Locate the P. falciparum-infected red blood cells and any of indeterminate infection status.
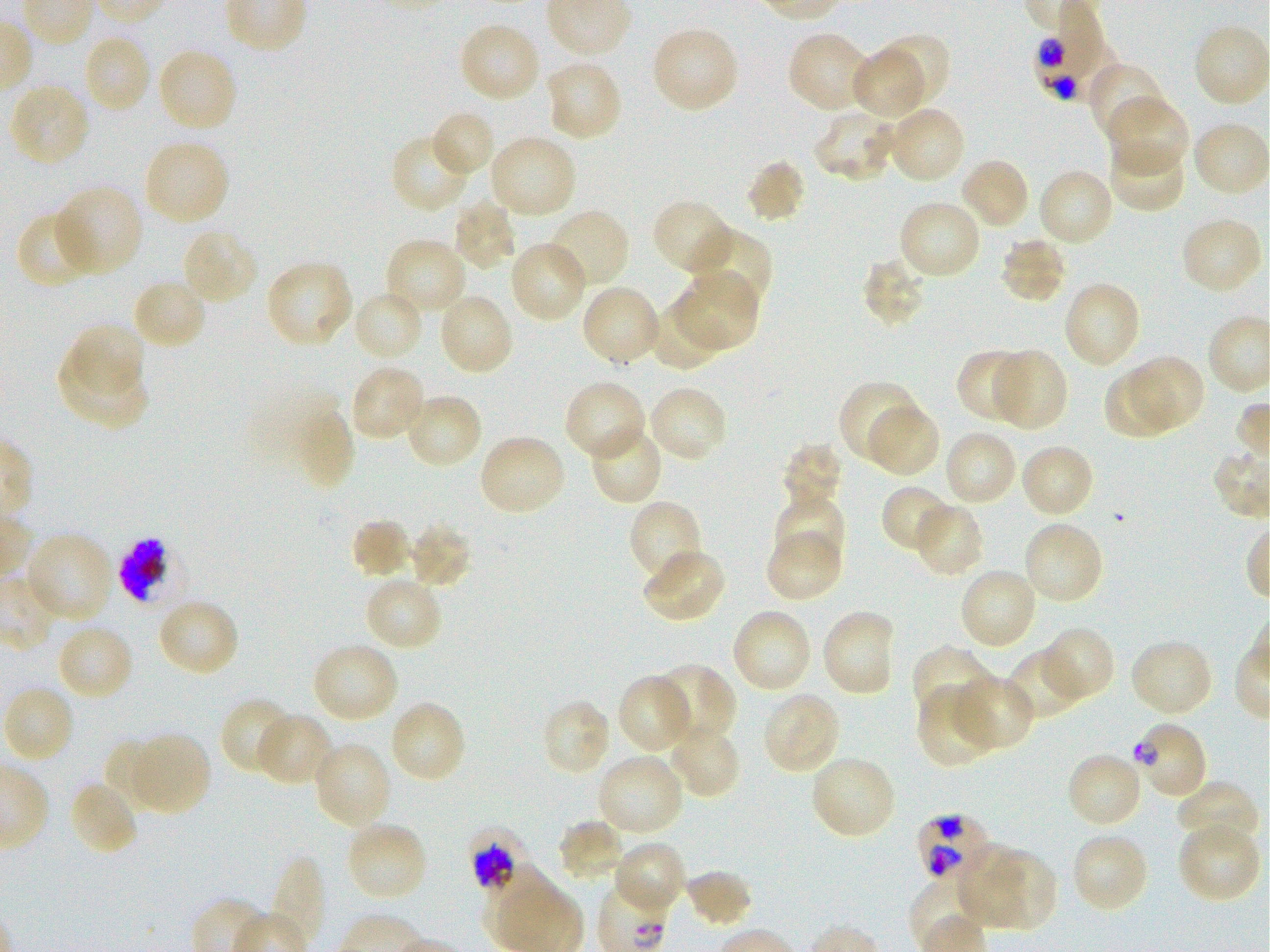
Approximate bounding rectangles given as corner coordinates in pixels from the top-left. Not every red blood cell is marked. A life-cycle stage — or a range of stages, where the recorded stages span more than one — follows each staged infected red blood cell.
Infected red blood cells: (x1=1035, y1=14, x2=1114, y2=102); (x1=1132, y1=721, x2=1208, y2=801) late ring to early trophozoite; (x1=914, y1=813, x2=995, y2=884); (x1=468, y1=826, x2=533, y2=895) early trophozoite to early schizont.
Red blood cells of indeterminate infection status: (x1=118, y1=536, x2=181, y2=607).

Locations of uninfected red blood cells: (x1=459, y1=21, x2=542, y2=104), (x1=1193, y1=23, x2=1269, y2=108), (x1=651, y1=26, x2=740, y2=114), (x1=786, y1=30, x2=871, y2=114), (x1=871, y1=31, x2=952, y2=107), (x1=81, y1=33, x2=152, y2=114), (x1=157, y1=48, x2=238, y2=132), (x1=848, y1=48, x2=924, y2=119), (x1=543, y1=60, x2=624, y2=141), (x1=1087, y1=61, x2=1169, y2=143), (x1=8, y1=83, x2=91, y2=167), (x1=1108, y1=96, x2=1191, y2=179), (x1=884, y1=106, x2=967, y2=185), (x1=811, y1=108, x2=897, y2=183), (x1=432, y1=114, x2=492, y2=174), (x1=1191, y1=121, x2=1268, y2=197), (x1=488, y1=134, x2=577, y2=219), (x1=142, y1=138, x2=230, y2=226), (x1=1107, y1=138, x2=1187, y2=214), (x1=395, y1=139, x2=466, y2=213), (x1=958, y1=156, x2=1031, y2=231), (x1=744, y1=158, x2=807, y2=225), (x1=1037, y1=167, x2=1115, y2=248), (x1=55, y1=184, x2=145, y2=276), (x1=451, y1=198, x2=518, y2=272), (x1=651, y1=199, x2=734, y2=277), (x1=897, y1=199, x2=982, y2=281), (x1=545, y1=208, x2=632, y2=290), (x1=16, y1=211, x2=98, y2=290), (x1=1180, y1=216, x2=1263, y2=295), (x1=689, y1=227, x2=774, y2=313), (x1=181, y1=228, x2=259, y2=306), (x1=998, y1=235, x2=1068, y2=305), (x1=383, y1=238, x2=466, y2=317), (x1=508, y1=240, x2=589, y2=324), (x1=859, y1=255, x2=928, y2=331), (x1=264, y1=259, x2=354, y2=349), (x1=674, y1=274, x2=760, y2=353), (x1=131, y1=277, x2=207, y2=352), (x1=1063, y1=280, x2=1142, y2=370), (x1=581, y1=285, x2=662, y2=367), (x1=352, y1=288, x2=426, y2=362), (x1=438, y1=292, x2=515, y2=377), (x1=646, y1=297, x2=723, y2=372), (x1=67, y1=323, x2=145, y2=396), (x1=956, y1=348, x2=1033, y2=423), (x1=991, y1=349, x2=1070, y2=432), (x1=57, y1=350, x2=150, y2=429), (x1=1127, y1=355, x2=1205, y2=431), (x1=348, y1=364, x2=426, y2=442), (x1=1101, y1=368, x2=1173, y2=441), (x1=563, y1=380, x2=646, y2=463), (x1=837, y1=381, x2=921, y2=464), (x1=645, y1=385, x2=728, y2=463), (x1=404, y1=392, x2=483, y2=469), (x1=866, y1=403, x2=940, y2=478), (x1=291, y1=407, x2=354, y2=490), (x1=588, y1=425, x2=664, y2=507), (x1=942, y1=429, x2=1018, y2=507), (x1=477, y1=434, x2=567, y2=518), (x1=780, y1=443, x2=844, y2=515), (x1=1019, y1=443, x2=1096, y2=520), (x1=880, y1=485, x2=958, y2=554), (x1=774, y1=494, x2=845, y2=566), (x1=629, y1=499, x2=703, y2=588), (x1=914, y1=502, x2=986, y2=578), (x1=350, y1=518, x2=413, y2=580), (x1=408, y1=520, x2=474, y2=590), (x1=1022, y1=520, x2=1105, y2=606), (x1=764, y1=528, x2=842, y2=602), (x1=25, y1=531, x2=114, y2=623), (x1=642, y1=549, x2=728, y2=625), (x1=958, y1=566, x2=1038, y2=651), (x1=363, y1=576, x2=443, y2=652), (x1=156, y1=597, x2=240, y2=679), (x1=731, y1=607, x2=813, y2=692), (x1=820, y1=608, x2=898, y2=698), (x1=55, y1=622, x2=135, y2=701), (x1=1038, y1=629, x2=1113, y2=697), (x1=1128, y1=638, x2=1214, y2=718), (x1=312, y1=643, x2=399, y2=725), (x1=910, y1=644, x2=996, y2=728), (x1=1005, y1=649, x2=1086, y2=721), (x1=651, y1=663, x2=737, y2=747), (x1=954, y1=673, x2=1034, y2=751), (x1=617, y1=674, x2=692, y2=754), (x1=2, y1=684, x2=75, y2=764), (x1=916, y1=687, x2=997, y2=769), (x1=761, y1=691, x2=841, y2=775), (x1=220, y1=697, x2=297, y2=777), (x1=389, y1=699, x2=467, y2=784), (x1=540, y1=699, x2=611, y2=776), (x1=255, y1=714, x2=334, y2=787), (x1=666, y1=722, x2=742, y2=800), (x1=127, y1=733, x2=211, y2=815), (x1=103, y1=738, x2=169, y2=809), (x1=312, y1=741, x2=392, y2=829), (x1=1065, y1=752, x2=1144, y2=830), (x1=595, y1=753, x2=684, y2=836), (x1=809, y1=754, x2=898, y2=841), (x1=67, y1=780, x2=139, y2=857), (x1=1175, y1=780, x2=1260, y2=851), (x1=557, y1=819, x2=626, y2=883), (x1=345, y1=820, x2=429, y2=902), (x1=1176, y1=820, x2=1261, y2=904), (x1=1071, y1=831, x2=1149, y2=913), (x1=958, y1=842, x2=1025, y2=926), (x1=615, y1=843, x2=684, y2=907), (x1=988, y1=851, x2=1055, y2=930), (x1=275, y1=856, x2=327, y2=940), (x1=684, y1=868, x2=753, y2=929). Static in-vitro culture of P. falciparum strain 3D7. Thin blood film. Donor blood group O+. 100x oil-immersion objective, numerical aperture 1.25. Image is 1270×952 pixels. Giemsa stain. Single field of view.